Assess this cell for malaria.
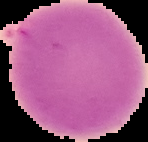
It is uninfected.

Summary:
  - Image type: cell region segmented out of the field of view; surrounding area masked to black
  - Preparation: thin blood film
  - Image size: 148×142 pixels